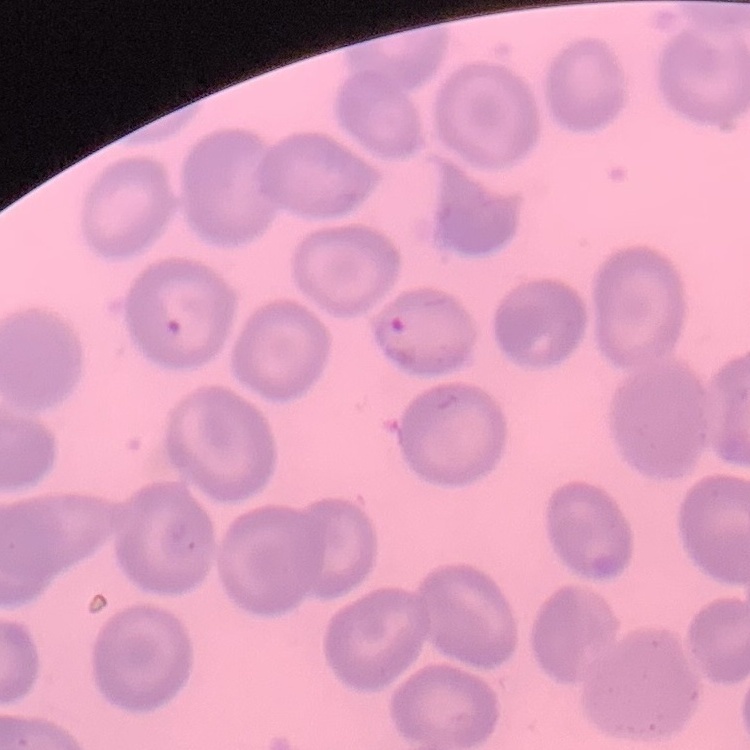

Summary:
  - Red blood cell morphology: no rouleaux formation
  - Stain: Field's or Giemsa
  - Preparation: thin blood film
  - Image type: one tile cut from a larger photomicrograph